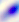

Summary:
  - Modality: micrograph
  - Identification: Toxoplasma gondii
  - Magnification: 400x